Assess this cell for malaria.
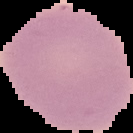

It is uninfected.

preparation = thin blood smear
image size = 133×133 pixels
image type = segmented cell region on a black background